Assess this cell for malaria.
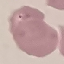
It is parasitized.

Summary:
  - Stain: Giemsa
  - Preparation: thin blood smear
  - Capture: smartphone camera at the microscope eyepiece
  - Image type: cell patch, automatically extracted from a larger field of view and resized to 64 × 64 pixels